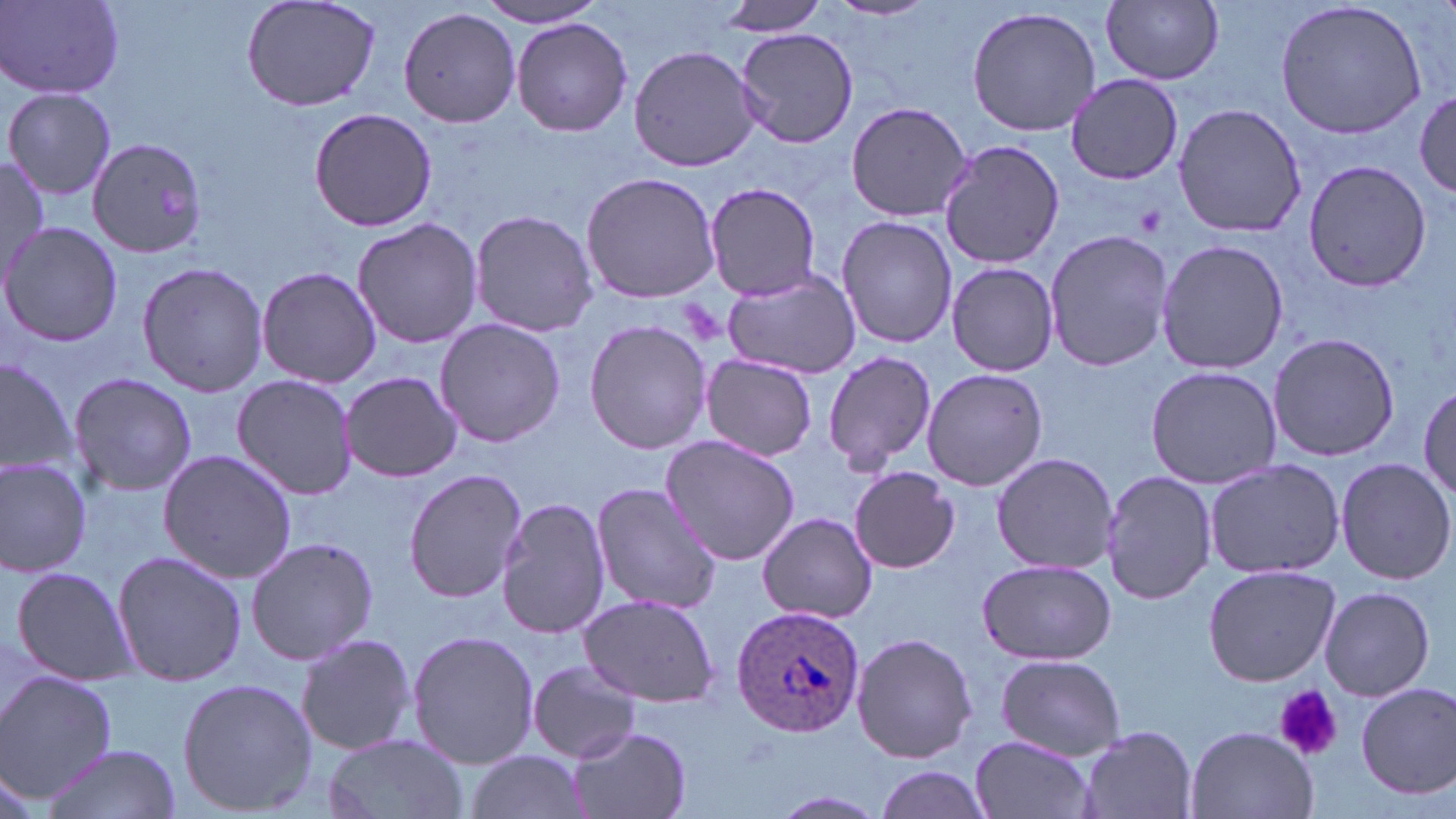

{
  "plasmodium_ovale_infected_red_blood_cell_locations": "approximate bounding boxes as (x1,y1)-(x2,y2) corner pairs in pixels: (728,603)-(863,739)",
  "slide_level_diagnosis": "Plasmodium ovale",
  "magnification": "1000x",
  "platelet_locations": "approximate bounding boxes as (x1,y1)-(x2,y2) corner pairs in pixels: (1132,201)-(1169,239), (1276,685)-(1342,762)",
  "image_size": "1456×819 pixels",
  "stain": "May-Grünwald-Giemsa",
  "modality": "light microscopy",
  "preparation": "thin blood smear",
  "uninfected_red_blood_cell_locations": "approximate bounding boxes as (x1,y1)-(x2,y2) corner pairs in pixels: (240,0)-(383,113), (712,0)-(832,38), (826,0)-(940,23), (1275,0)-(1430,140), (1101,1)-(1226,85), (474,2)-(608,27), (3,3)-(123,99), (965,5)-(1102,138), (399,6)-(521,128), (511,17)-(633,137), (735,27)-(857,150), (629,45)-(763,173), (1065,72)-(1184,187), (2,87)-(116,202), (1415,89)-(1454,197), (844,101)-(974,223), (1172,101)-(1307,238), (308,106)-(439,231), (938,137)-(1064,271), (87,138)-(211,261), (0,157)-(51,284), (1302,160)-(1432,292), (581,170)-(721,304), (704,182)-(823,300), (468,209)-(598,338), (835,214)-(957,350), (352,216)-(482,349), (0,221)-(122,349), (1044,229)-(1173,374), (1155,238)-(1288,376), (136,260)-(269,396), (946,261)-(1060,377), (256,264)-(381,388), (720,268)-(864,378), (435,318)-(565,448), (583,318)-(711,455), (1267,331)-(1401,463), (821,348)-(937,474), (700,354)-(819,460), (0,355)-(81,484), (1144,365)-(1281,488), (921,368)-(1049,493), (341,371)-(462,482), (68,372)-(197,498), (233,375)-(359,500), (1418,381)-(1455,510), (660,436)-(802,567), (157,449)-(298,582), (989,452)-(1117,574), (0,457)-(93,577), (1335,457)-(1454,584), (1202,459)-(1347,578), (846,467)-(962,572), (403,468)-(527,602), (1101,468)-(1214,606), (589,482)-(721,614), (497,496)-(613,641), (757,511)-(879,623), (244,535)-(378,666), (111,549)-(250,687), (976,558)-(1116,666), (1201,564)-(1340,686), (7,565)-(136,683), (1319,586)-(1435,700), (578,593)-(720,708), (407,631)-(538,770), (294,633)-(416,756), (849,633)-(979,765), (994,655)-(1126,760), (526,660)-(644,763), (1,672)-(117,801), (176,677)-(316,818), (1356,682)-(1456,799), (1185,725)-(1318,819), (566,726)-(691,819), (1076,726)-(1197,819), (320,732)-(467,819), (968,735)-(1097,819), (40,743)-(182,818), (463,749)-(590,819), (867,764)-(995,819), (765,791)-(895,818)",
  "field_of_view": "single"
}